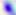
Summary:
  - Identification: Toxoplasma gondii
  - Modality: micrograph
  - Magnification: 400x